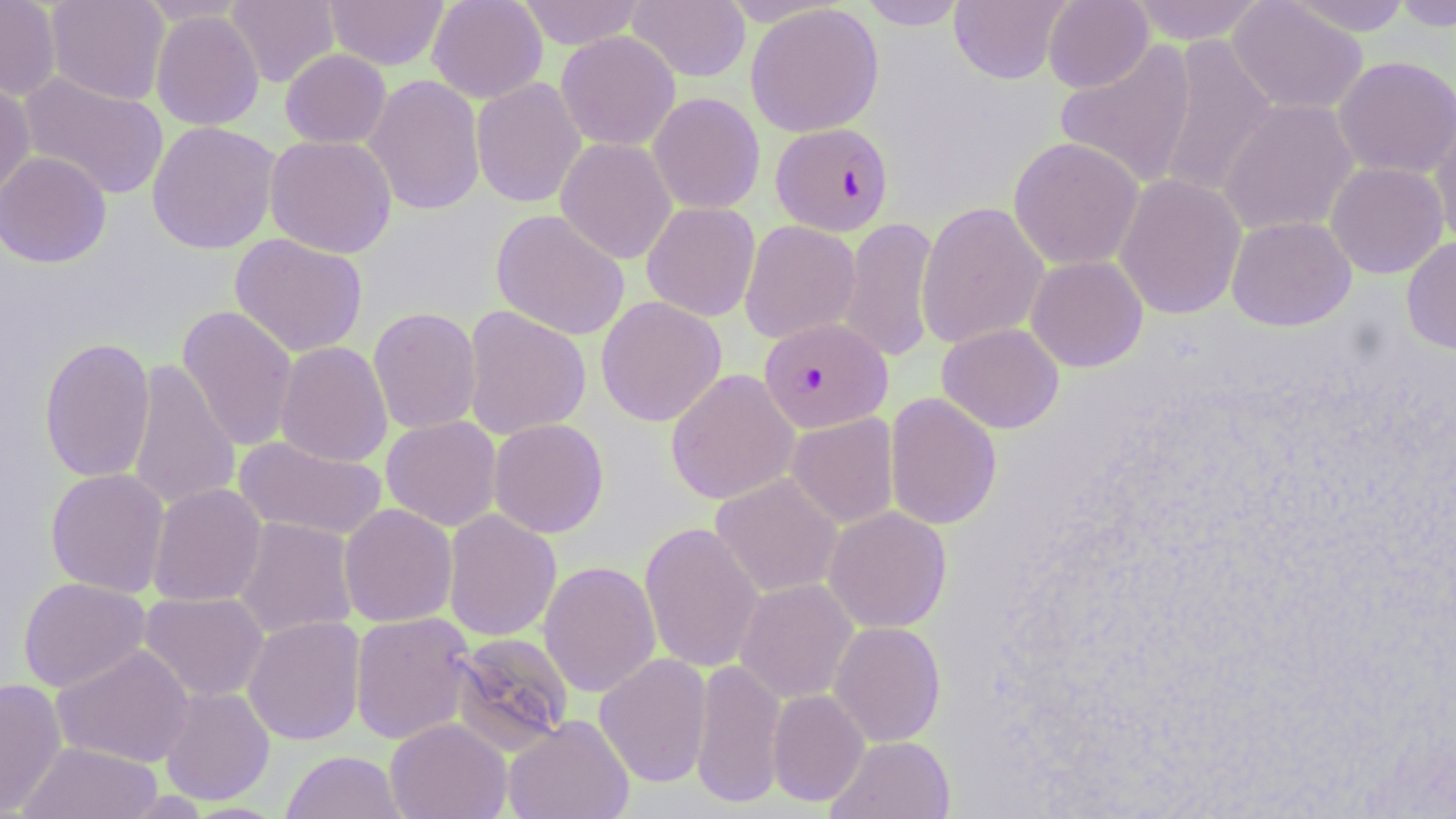

slide-level diagnosis = Plasmodium falciparum
field of view = one of a larger specimen
image size = 1456×819 pixels
Plasmodium falciparum-infected red blood cell locations = approximate bounding boxes as [x1, y1, x2, y2] in pixels: [770, 122, 894, 236], [758, 317, 892, 433]
magnification = 1000x
modality = light microscopy
stain = May-Grünwald-Giemsa
preparation = thin blood film
uninfected red blood cell locations = approximate bounding boxes as [x1, y1, x2, y2] in pixels: [0, 0, 61, 101], [46, 0, 170, 106], [226, 0, 340, 88], [325, 0, 449, 70], [427, 0, 548, 103], [515, 0, 647, 49], [627, 0, 750, 82], [858, 0, 968, 30], [949, 0, 1070, 84], [1042, 0, 1153, 93], [1128, 0, 1268, 44], [1283, 0, 1413, 36], [1389, 0, 1456, 32], [1227, 1, 1368, 116], [745, 3, 884, 137], [150, 9, 265, 131], [555, 31, 681, 151], [1155, 35, 1277, 200], [1054, 40, 1198, 188], [280, 48, 392, 149], [1333, 55, 1456, 178], [18, 71, 169, 201], [364, 74, 486, 216], [0, 77, 36, 205], [471, 77, 587, 208], [648, 92, 765, 214], [1216, 99, 1359, 237], [1429, 116, 1456, 247], [146, 121, 281, 255], [265, 134, 398, 258], [555, 137, 677, 264], [1008, 137, 1144, 270], [0, 151, 111, 268], [1325, 161, 1448, 279], [1114, 174, 1247, 320], [641, 201, 760, 321], [916, 201, 1049, 349], [491, 209, 631, 341], [1226, 215, 1356, 331], [838, 217, 940, 363], [739, 220, 861, 344], [229, 233, 368, 357], [1401, 236, 1456, 354], [1026, 255, 1148, 372], [595, 296, 727, 427], [177, 305, 298, 452], [462, 305, 591, 441], [368, 307, 482, 434], [937, 323, 1064, 433], [38, 337, 156, 483], [275, 341, 393, 468], [126, 358, 240, 513], [665, 368, 800, 505], [884, 392, 1002, 531], [787, 413, 899, 528], [381, 415, 502, 531], [488, 418, 609, 538], [233, 435, 388, 541], [45, 468, 170, 597], [710, 473, 844, 598], [147, 483, 267, 607], [338, 504, 458, 627], [823, 506, 952, 633], [442, 509, 561, 641], [233, 517, 358, 639], [639, 521, 765, 674], [539, 560, 661, 698], [18, 577, 151, 693], [735, 578, 858, 704], [139, 591, 268, 701], [350, 612, 476, 745], [243, 615, 366, 745], [828, 621, 946, 747], [448, 632, 575, 755], [51, 644, 195, 768], [594, 653, 712, 788], [691, 658, 786, 808], [0, 678, 66, 816], [159, 686, 275, 805], [767, 689, 869, 806], [503, 714, 634, 819], [385, 717, 512, 819], [826, 735, 956, 819], [18, 741, 163, 819], [281, 750, 406, 819]